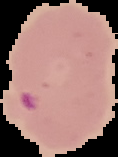

image size = 118×157 pixels
malaria status = parasitized
preparation = thin blood smear
image type = segmented cell region with the area outside set to black